Locate every Plasmodium vivax-infected red blood cell.
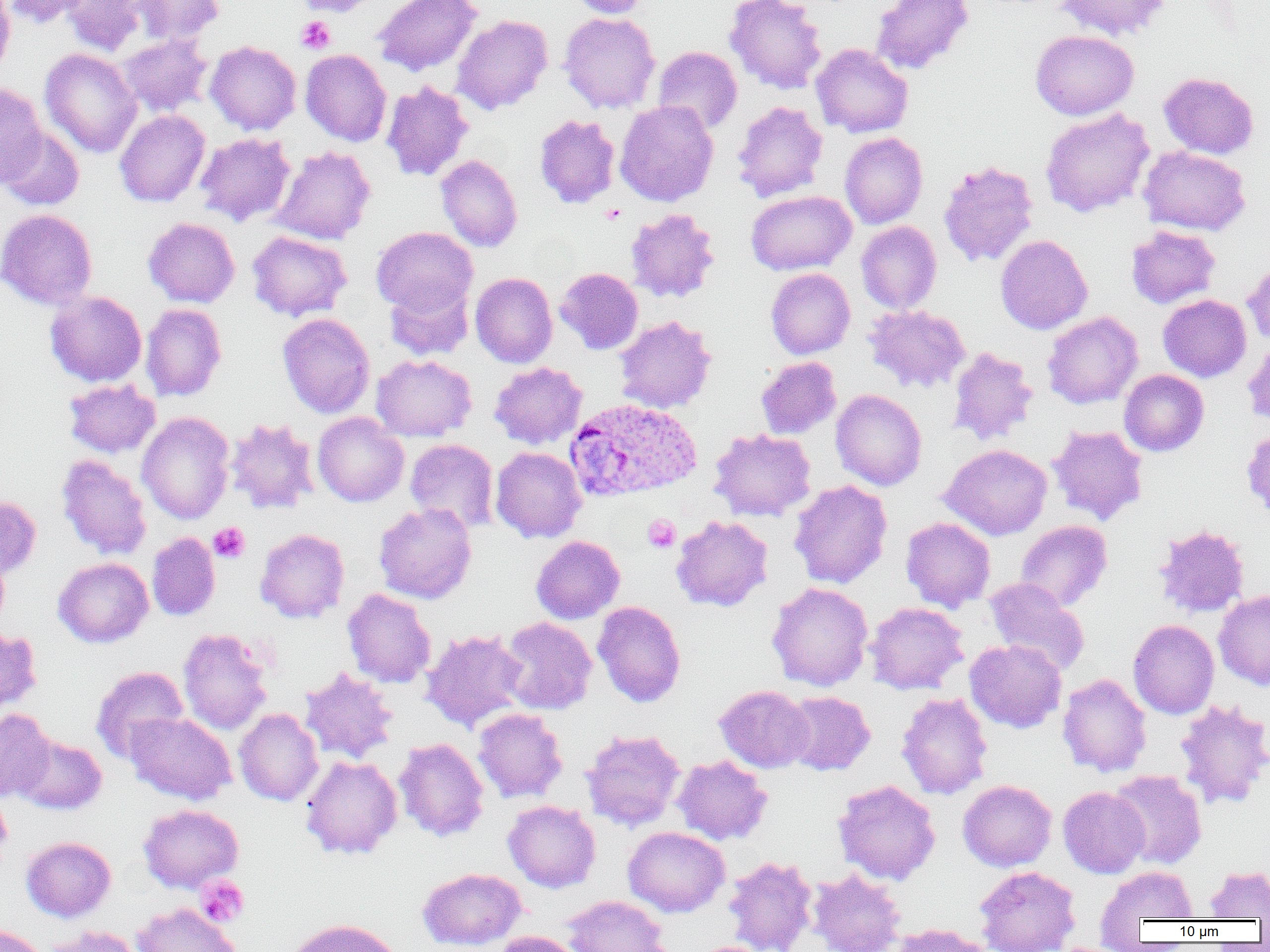
Approximate bounding boxes as named x1/y1/x2/y2 corners in pixels.
Plasmodium vivax-infected red blood cells: (x1=563, y1=398, x2=702, y2=503).

Summary:
  - Uninfected red blood cell locations: (x1=4, y1=0, x2=90, y2=29), (x1=61, y1=0, x2=154, y2=57), (x1=134, y1=0, x2=224, y2=45), (x1=294, y1=0, x2=381, y2=16), (x1=373, y1=0, x2=482, y2=77), (x1=564, y1=0, x2=650, y2=18), (x1=724, y1=0, x2=827, y2=94), (x1=871, y1=0, x2=974, y2=75), (x1=1053, y1=0, x2=1171, y2=41), (x1=0, y1=1, x2=15, y2=78), (x1=558, y1=12, x2=660, y2=113), (x1=452, y1=14, x2=553, y2=114), (x1=1030, y1=29, x2=1139, y2=119), (x1=119, y1=34, x2=212, y2=117), (x1=205, y1=41, x2=301, y2=135), (x1=810, y1=43, x2=914, y2=138), (x1=653, y1=46, x2=742, y2=134), (x1=39, y1=48, x2=142, y2=157), (x1=300, y1=49, x2=391, y2=146), (x1=292, y1=50, x2=381, y2=244), (x1=1158, y1=72, x2=1259, y2=159), (x1=382, y1=81, x2=474, y2=182), (x1=0, y1=82, x2=48, y2=188), (x1=615, y1=100, x2=718, y2=206), (x1=732, y1=101, x2=828, y2=203), (x1=1040, y1=108, x2=1154, y2=217), (x1=115, y1=110, x2=210, y2=207), (x1=534, y1=114, x2=620, y2=208), (x1=0, y1=126, x2=84, y2=211), (x1=195, y1=132, x2=295, y2=227), (x1=839, y1=132, x2=928, y2=229), (x1=270, y1=146, x2=376, y2=245), (x1=1139, y1=146, x2=1251, y2=236), (x1=436, y1=155, x2=522, y2=252), (x1=938, y1=161, x2=1038, y2=267), (x1=746, y1=190, x2=856, y2=275), (x1=626, y1=207, x2=720, y2=302), (x1=0, y1=208, x2=97, y2=310), (x1=143, y1=217, x2=240, y2=308), (x1=856, y1=221, x2=942, y2=314), (x1=1126, y1=225, x2=1220, y2=309), (x1=371, y1=226, x2=477, y2=315), (x1=247, y1=230, x2=352, y2=321), (x1=995, y1=235, x2=1093, y2=334), (x1=1242, y1=258, x2=1270, y2=346), (x1=555, y1=267, x2=643, y2=354), (x1=765, y1=268, x2=855, y2=359), (x1=470, y1=272, x2=557, y2=367), (x1=385, y1=280, x2=474, y2=361), (x1=45, y1=291, x2=146, y2=387), (x1=1158, y1=294, x2=1252, y2=382), (x1=140, y1=303, x2=227, y2=401), (x1=865, y1=304, x2=970, y2=393), (x1=1042, y1=311, x2=1143, y2=409), (x1=277, y1=313, x2=375, y2=418), (x1=615, y1=315, x2=716, y2=413), (x1=1241, y1=338, x2=1270, y2=428), (x1=948, y1=347, x2=1038, y2=445), (x1=371, y1=354, x2=476, y2=441), (x1=756, y1=356, x2=841, y2=439), (x1=489, y1=362, x2=587, y2=450), (x1=1119, y1=369, x2=1209, y2=456), (x1=64, y1=379, x2=160, y2=458), (x1=831, y1=389, x2=927, y2=491), (x1=136, y1=411, x2=235, y2=524), (x1=312, y1=412, x2=409, y2=507), (x1=225, y1=418, x2=320, y2=515), (x1=1047, y1=424, x2=1149, y2=525), (x1=1241, y1=425, x2=1270, y2=521), (x1=709, y1=428, x2=816, y2=521), (x1=405, y1=438, x2=499, y2=533), (x1=939, y1=444, x2=1052, y2=540), (x1=490, y1=447, x2=587, y2=543), (x1=56, y1=455, x2=152, y2=560), (x1=788, y1=480, x2=892, y2=589), (x1=0, y1=495, x2=42, y2=580), (x1=373, y1=502, x2=477, y2=604), (x1=671, y1=515, x2=773, y2=612), (x1=901, y1=517, x2=996, y2=612), (x1=1015, y1=520, x2=1113, y2=611), (x1=1153, y1=524, x2=1249, y2=618), (x1=255, y1=528, x2=349, y2=623), (x1=147, y1=532, x2=220, y2=621), (x1=531, y1=535, x2=625, y2=624), (x1=0, y1=548, x2=10, y2=632), (x1=53, y1=557, x2=153, y2=648), (x1=983, y1=578, x2=1090, y2=675), (x1=767, y1=582, x2=873, y2=691), (x1=342, y1=588, x2=436, y2=688), (x1=1214, y1=590, x2=1270, y2=690), (x1=592, y1=601, x2=686, y2=707), (x1=865, y1=602, x2=968, y2=694), (x1=498, y1=616, x2=597, y2=715), (x1=1128, y1=619, x2=1219, y2=719), (x1=0, y1=627, x2=42, y2=715), (x1=178, y1=627, x2=273, y2=735), (x1=421, y1=629, x2=528, y2=731), (x1=964, y1=640, x2=1067, y2=733), (x1=90, y1=665, x2=188, y2=763), (x1=299, y1=667, x2=398, y2=764), (x1=1057, y1=672, x2=1152, y2=777), (x1=714, y1=685, x2=814, y2=773), (x1=783, y1=691, x2=875, y2=775), (x1=896, y1=692, x2=993, y2=800), (x1=1174, y1=699, x2=1270, y2=810), (x1=234, y1=708, x2=323, y2=806), (x1=472, y1=708, x2=567, y2=803), (x1=0, y1=709, x2=55, y2=802), (x1=125, y1=711, x2=236, y2=804), (x1=581, y1=729, x2=685, y2=831), (x1=13, y1=734, x2=107, y2=815), (x1=394, y1=738, x2=489, y2=842), (x1=300, y1=754, x2=403, y2=860), (x1=672, y1=755, x2=773, y2=845), (x1=1109, y1=770, x2=1207, y2=870), (x1=833, y1=779, x2=941, y2=885), (x1=958, y1=779, x2=1057, y2=872), (x1=1058, y1=786, x2=1150, y2=878), (x1=0, y1=796, x2=12, y2=858), (x1=503, y1=800, x2=600, y2=893), (x1=138, y1=804, x2=244, y2=893), (x1=623, y1=826, x2=729, y2=917), (x1=20, y1=836, x2=116, y2=922), (x1=723, y1=855, x2=817, y2=952), (x1=1204, y1=864, x2=1270, y2=919), (x1=974, y1=865, x2=1081, y2=952), (x1=1096, y1=866, x2=1198, y2=931), (x1=417, y1=868, x2=527, y2=950), (x1=808, y1=869, x2=906, y2=952), (x1=561, y1=895, x2=668, y2=952), (x1=132, y1=903, x2=241, y2=952), (x1=284, y1=918, x2=404, y2=952), (x1=0, y1=923, x2=48, y2=952), (x1=887, y1=923, x2=993, y2=952), (x1=42, y1=926, x2=143, y2=952), (x1=491, y1=931, x2=584, y2=952)
  - Platelet locations: (x1=296, y1=16, x2=336, y2=54), (x1=643, y1=514, x2=680, y2=551), (x1=209, y1=522, x2=250, y2=563), (x1=195, y1=876, x2=249, y2=927)
  - Slide-level diagnosis: Plasmodium vivax
  - Image size: 1270×952 pixels
  - Preparation: thin blood smear
  - Modality: optical microscopy
  - Field of view: single
  - Magnification: 1000x